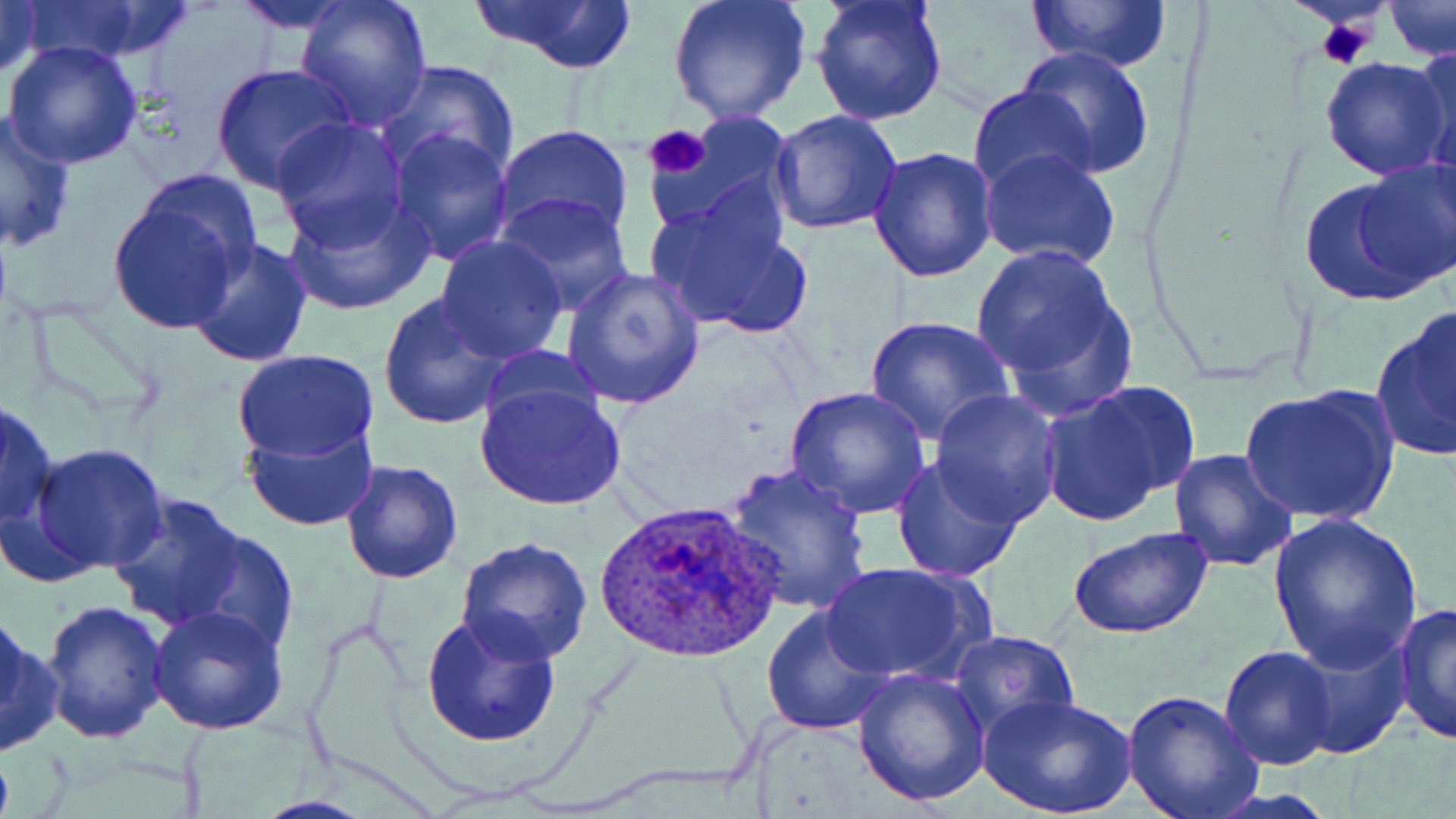

Summary:
  - Coordinate format: approximate bounding boxes as [x1, y1, x2, y2] in pixels
  - Uninfected red blood cell locations: [0, 0, 44, 83], [14, 0, 198, 68], [224, 0, 368, 35], [467, 0, 639, 73], [667, 0, 812, 126], [811, 0, 949, 126], [1030, 0, 1171, 73], [293, 1, 434, 130], [1383, 2, 1455, 61], [2, 39, 145, 171], [1407, 40, 1456, 177], [1018, 45, 1156, 177], [1319, 54, 1454, 180], [377, 60, 520, 180], [212, 62, 356, 193], [968, 85, 1098, 197], [0, 109, 77, 252], [769, 110, 902, 234], [642, 114, 797, 238], [269, 115, 410, 248], [493, 125, 635, 247], [387, 127, 515, 266], [869, 145, 999, 283], [978, 145, 1122, 271], [1354, 154, 1456, 288], [133, 170, 265, 290], [1295, 173, 1444, 306], [643, 186, 808, 337], [281, 190, 435, 316], [495, 192, 636, 316], [104, 193, 249, 335], [433, 234, 568, 364], [184, 236, 315, 369], [968, 240, 1139, 413], [562, 267, 705, 410], [377, 293, 513, 432], [1368, 305, 1455, 464], [865, 315, 1014, 446], [476, 346, 608, 436], [231, 349, 379, 464], [474, 377, 628, 511], [1039, 382, 1193, 526], [785, 385, 930, 519], [1239, 387, 1399, 526], [930, 388, 1062, 526], [1, 397, 60, 530], [242, 415, 379, 531], [28, 443, 172, 574], [1167, 449, 1299, 573], [889, 452, 1026, 583], [340, 458, 465, 584], [722, 461, 873, 617], [107, 493, 255, 635], [1267, 514, 1423, 669], [181, 524, 301, 658], [1069, 528, 1212, 641], [456, 535, 591, 665], [821, 562, 985, 683], [37, 600, 168, 745], [1393, 600, 1456, 745], [147, 604, 290, 736], [760, 607, 893, 734], [420, 610, 564, 749], [0, 616, 60, 758], [1285, 629, 1413, 760], [949, 630, 1080, 744], [883, 636, 1073, 803], [1219, 644, 1339, 769], [851, 668, 990, 808], [1121, 689, 1262, 819], [978, 693, 1138, 818]
  - Plasmodium ovale-infected red blood cell locations: [594, 498, 782, 665]
  - Platelet locations: [1314, 17, 1376, 69], [644, 124, 712, 180]
  - Slide-level diagnosis: Plasmodium ovale
  - Modality: light microscopy
  - Field of view: one of a larger specimen
  - Magnification: 1000x
  - Preparation: thin blood film
  - Stain: May-Grünwald-Giemsa
  - Image size: 1456×819 pixels